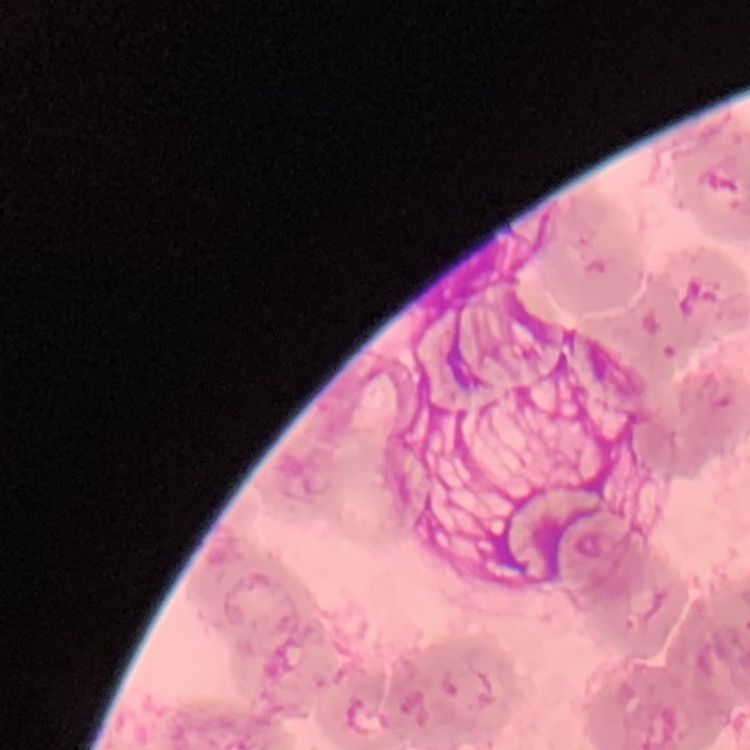
Summary:
  - Red blood cell morphology: rouleaux formation
  - Image type: one tile cut from a larger photomicrograph
  - Stain: Field's or Giemsa
  - Preparation: thin blood smear